State the blood parasite species.
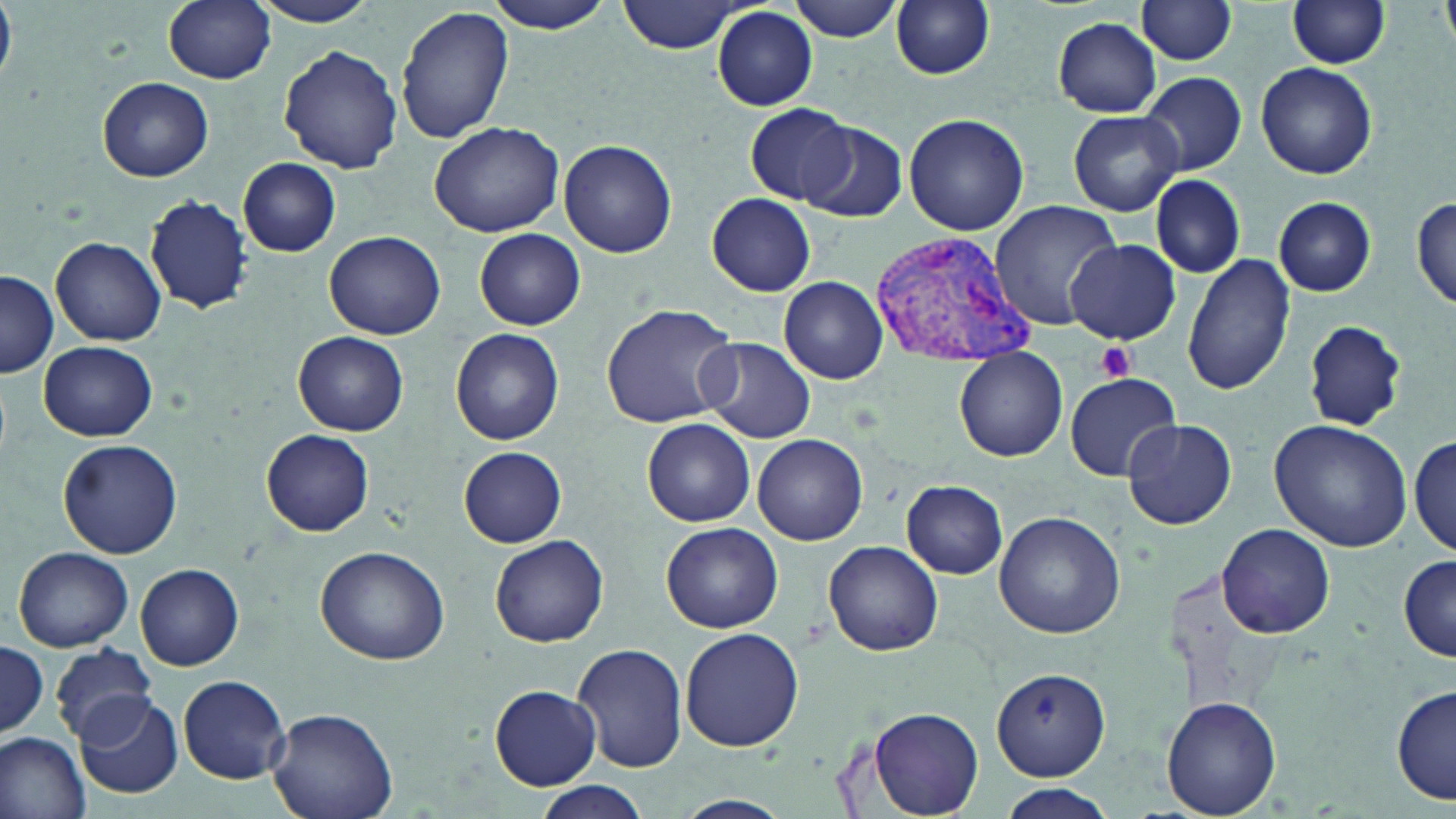
Plasmodium vivax.

Approximate bounding boxes as [x1, y1, x2, y2] in pixels. Platelet locations: [1096, 341, 1135, 381]. Plasmodium vivax-infected red blood cell locations: [869, 225, 1039, 366]. Uninfected red blood cell locations: [0, 0, 16, 78], [163, 0, 275, 85], [250, 0, 382, 27], [484, 0, 619, 33], [619, 0, 746, 54], [787, 0, 909, 41], [891, 1, 996, 79], [1138, 1, 1238, 65], [1286, 1, 1394, 69], [395, 6, 514, 145], [712, 8, 817, 111], [1051, 17, 1162, 117], [278, 44, 402, 175], [1255, 62, 1377, 179], [1139, 72, 1247, 177], [98, 77, 213, 181], [741, 106, 856, 206], [1066, 109, 1185, 216], [903, 112, 1030, 236], [798, 119, 909, 222], [429, 122, 564, 236], [558, 138, 678, 258], [238, 157, 341, 257], [1149, 176, 1247, 280], [146, 193, 250, 315], [707, 193, 817, 295], [1411, 196, 1455, 311], [1273, 197, 1376, 297], [989, 199, 1123, 331], [475, 228, 585, 330], [325, 230, 446, 340], [50, 236, 167, 346], [1067, 238, 1180, 345], [1183, 252, 1296, 398], [0, 271, 59, 378], [778, 277, 887, 384], [600, 303, 739, 428], [1302, 319, 1407, 430], [450, 328, 565, 445], [294, 331, 408, 435], [698, 337, 816, 443], [39, 342, 157, 440], [952, 350, 1067, 464], [1064, 372, 1181, 480], [642, 418, 756, 528], [1120, 418, 1237, 530], [1269, 419, 1412, 552], [262, 429, 375, 537], [1411, 432, 1454, 560], [753, 434, 867, 544], [58, 437, 183, 559], [459, 446, 568, 548], [902, 479, 1007, 577], [994, 511, 1127, 640], [662, 522, 782, 634], [1217, 523, 1336, 639], [489, 535, 608, 649], [823, 542, 943, 655], [12, 545, 133, 652], [315, 545, 450, 665], [1396, 553, 1456, 661], [136, 563, 244, 671], [677, 626, 804, 754], [0, 640, 47, 741], [570, 642, 688, 773], [49, 643, 156, 746], [990, 666, 1110, 781], [178, 675, 291, 783], [1391, 682, 1456, 808], [488, 686, 602, 789], [74, 694, 181, 799], [1165, 695, 1283, 817], [867, 706, 984, 818], [266, 707, 399, 819], [0, 731, 92, 819], [994, 783, 1118, 818], [534, 784, 650, 817], [672, 795, 793, 819]. May-Grünwald-Giemsa-stained preparation. Image is 1456×819 pixels. Optical microscopy. One field of a larger specimen. Captured at 1000x magnification. Thin blood smear.